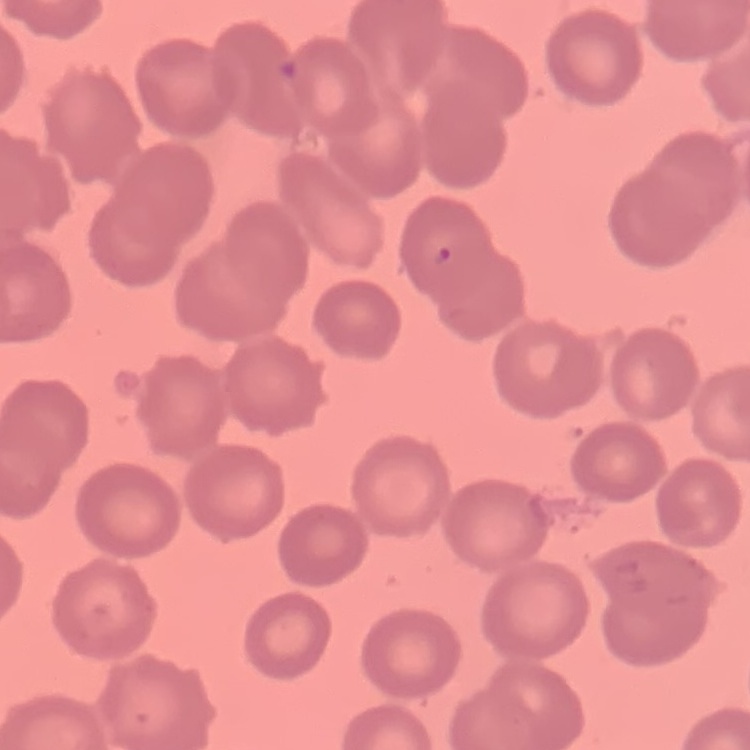

The erythrocytes exhibit no rouleaux formation. One tile cut from a larger photomicrograph. Field's or Giemsa stain. Thin blood film.